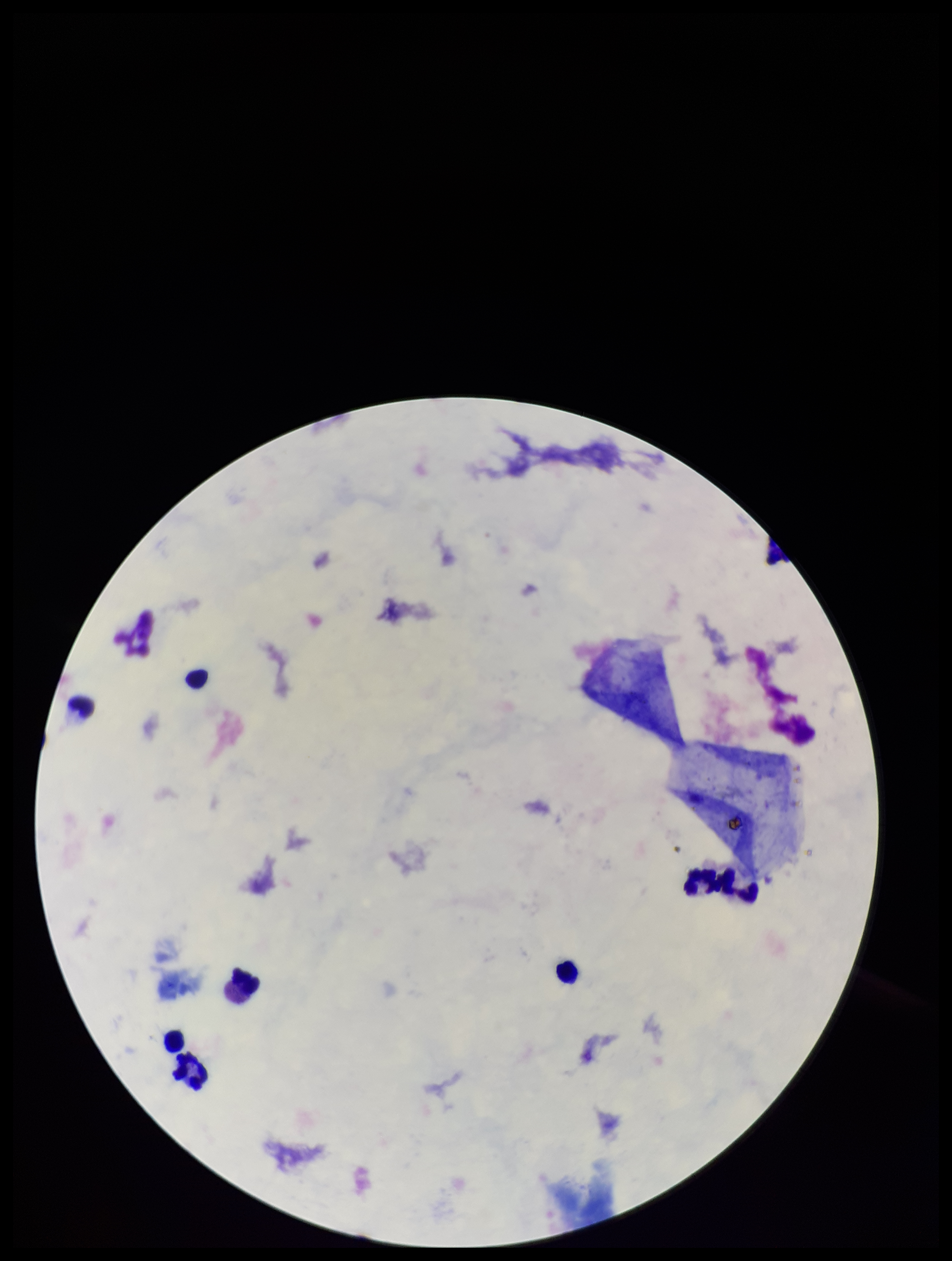 Plasmodium parasites: none identified. Leukocyte count: 7. Single field of view. Patient malaria status: negative. Smartphone photograph taken through the eyepiece of a microscope. Stained with Giemsa. Image is 952×1261 pixels. Preparation: thick blood smear. Parasite count: 0.